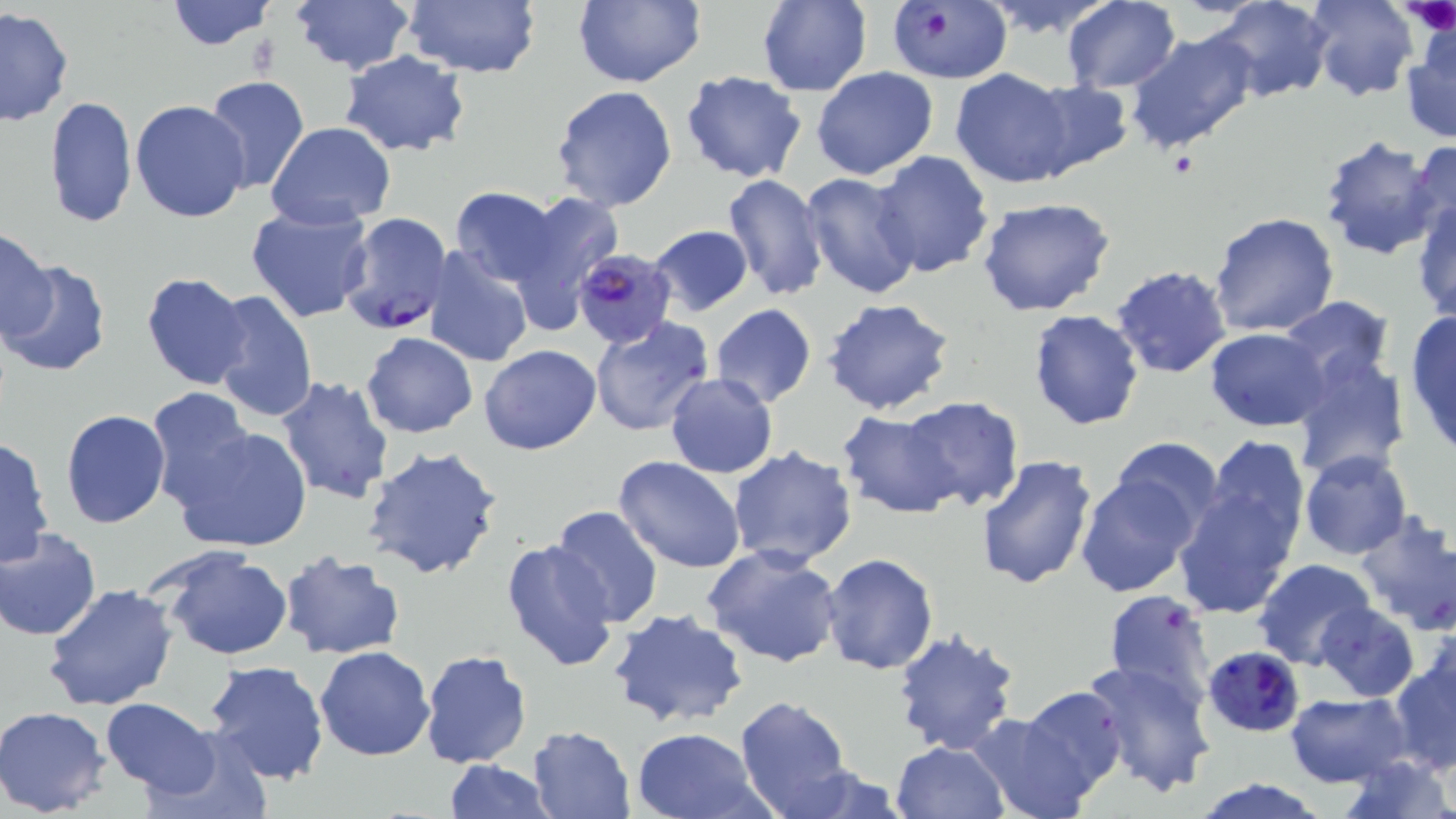

Approximate bounding boxes as (x1,y1)-(x2,y2) corner pairs in pixels. Uninfected red blood cell locations: (164,0)-(276,50), (401,0)-(541,76), (571,0)-(705,89), (757,0)-(871,96), (988,0)-(1108,35), (1062,0)-(1180,92), (1208,0)-(1334,103), (1304,0)-(1417,100), (291,1)-(415,75), (0,8)-(74,126), (1400,24)-(1456,144), (1125,30)-(1256,154), (339,51)-(471,157), (811,67)-(941,181), (951,69)-(1077,188), (680,71)-(806,183), (202,75)-(311,196), (1024,81)-(1131,176), (549,84)-(678,213), (44,95)-(137,228), (131,100)-(252,223), (267,122)-(397,229), (1316,136)-(1441,261), (1405,139)-(1456,249), (868,150)-(996,280), (800,172)-(920,298), (721,174)-(829,301), (450,186)-(561,289), (507,190)-(624,328), (1411,196)-(1456,327), (975,197)-(1117,318), (245,203)-(375,322), (1207,211)-(1339,338), (647,225)-(754,316), (0,227)-(57,342), (424,245)-(535,368), (1,261)-(110,379), (1111,265)-(1232,379), (140,273)-(252,389), (208,288)-(318,423), (1276,295)-(1394,391), (823,297)-(957,416), (711,304)-(817,408), (1027,308)-(1144,430), (1405,311)-(1456,453), (588,317)-(717,438), (1206,328)-(1330,431), (361,331)-(479,439), (479,345)-(601,455), (1290,350)-(1411,482), (665,373)-(778,479), (277,376)-(395,504), (144,389)-(262,512), (901,397)-(1025,511), (60,410)-(171,528), (837,411)-(962,519), (170,422)-(313,553), (1197,434)-(1311,566), (0,436)-(55,568), (1105,436)-(1226,539), (363,445)-(504,581), (727,446)-(858,568), (1298,451)-(1412,561), (976,454)-(1097,591), (615,456)-(745,573), (1076,473)-(1199,596), (1171,477)-(1301,618), (550,505)-(664,627), (1354,511)-(1456,633), (1,528)-(101,641), (500,538)-(619,672), (154,544)-(295,661), (705,545)-(843,668), (277,550)-(404,660), (821,553)-(938,674), (1255,560)-(1378,669), (43,583)-(178,712), (1101,589)-(1217,708), (1316,603)-(1419,702), (607,607)-(749,728), (892,627)-(1021,757), (315,646)-(435,762), (420,648)-(533,769), (1389,654)-(1455,775), (1081,657)-(1215,797), (203,660)-(330,787), (1015,684)-(1128,802), (1284,690)-(1411,788), (734,695)-(853,819), (101,697)-(220,797), (1,707)-(111,816), (968,711)-(1097,819), (526,725)-(635,818), (145,727)-(272,819), (629,728)-(764,818), (890,741)-(1009,819), (1342,757)-(1453,819), (442,760)-(552,818), (780,765)-(911,819), (1187,778)-(1332,818). Platelet locations: (1400,0)-(1456,36). Plasmodium falciparum-infected red blood cell locations: (886,0)-(1011,84), (339,212)-(453,338), (573,247)-(677,348), (1203,644)-(1304,738). Slide-level diagnosis: Plasmodium falciparum. Single field of view. Image is 1456×819 pixels. May-Grünwald-Giemsa stain. Thin blood film. Captured at 1000x magnification. Optical microscopy.